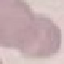
{
  "result": "no malaria parasites seen",
  "stain": "Giemsa",
  "capture": "smartphone through the microscope eyepiece",
  "preparation": "thin blood smear",
  "image_type": "cell patch, automatically extracted from a larger field of view and resized to 64 × 64 pixels"
}